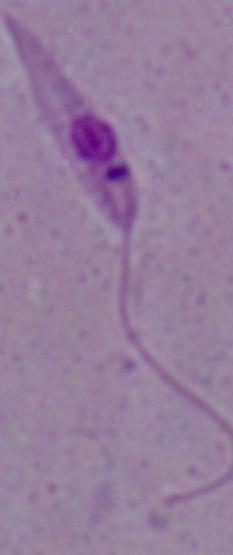
Micrograph. Captured at 1000x magnification. A Leishmania parasite is seen.